Report the malaria status of this cell.
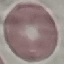
Uninfected.

capture: smartphone camera at the microscope eyepiece
stain: Giemsa
image_type: automatically extracted cell patch, resized to 64 × 64 pixels
preparation: thin blood smear